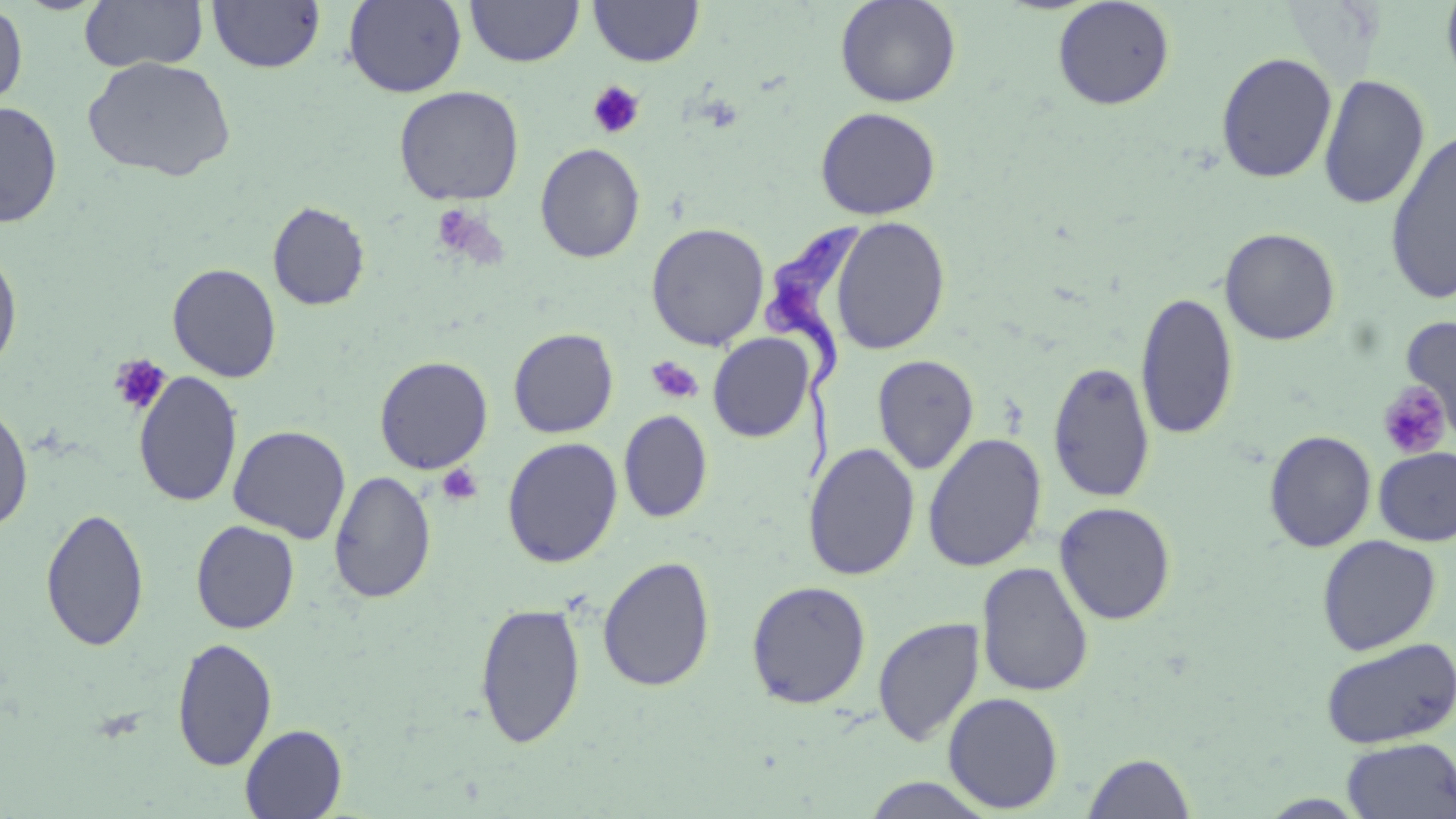
Approximate bounding boxes as named x1/y1/x2/y2 corners in pixels. Uninfected red blood cell locations: (x1=80, y1=0, x2=208, y2=72), (x1=207, y1=0, x2=326, y2=74), (x1=343, y1=0, x2=468, y2=98), (x1=465, y1=0, x2=583, y2=67), (x1=834, y1=0, x2=962, y2=107), (x1=1052, y1=0, x2=1175, y2=111), (x1=1441, y1=0, x2=1456, y2=93), (x1=589, y1=1, x2=704, y2=67), (x1=0, y1=3, x2=28, y2=109), (x1=1215, y1=51, x2=1337, y2=183), (x1=81, y1=56, x2=237, y2=182), (x1=1318, y1=73, x2=1431, y2=210), (x1=393, y1=85, x2=524, y2=206), (x1=0, y1=99, x2=63, y2=229), (x1=814, y1=106, x2=941, y2=220), (x1=1384, y1=127, x2=1456, y2=306), (x1=535, y1=142, x2=645, y2=263), (x1=267, y1=201, x2=370, y2=311), (x1=830, y1=216, x2=951, y2=356), (x1=646, y1=222, x2=770, y2=350), (x1=1219, y1=227, x2=1341, y2=346), (x1=0, y1=246, x2=23, y2=375), (x1=166, y1=263, x2=281, y2=383), (x1=1135, y1=291, x2=1238, y2=441), (x1=1398, y1=316, x2=1456, y2=442), (x1=508, y1=328, x2=618, y2=438), (x1=708, y1=333, x2=814, y2=442), (x1=872, y1=354, x2=979, y2=475), (x1=374, y1=355, x2=493, y2=474), (x1=1047, y1=361, x2=1155, y2=503), (x1=133, y1=372, x2=243, y2=508), (x1=0, y1=400, x2=34, y2=533), (x1=619, y1=409, x2=713, y2=523), (x1=228, y1=424, x2=351, y2=543), (x1=1263, y1=430, x2=1377, y2=553), (x1=922, y1=432, x2=1047, y2=573), (x1=501, y1=437, x2=623, y2=568), (x1=803, y1=443, x2=921, y2=581), (x1=1373, y1=447, x2=1456, y2=546), (x1=328, y1=470, x2=436, y2=604), (x1=1054, y1=501, x2=1177, y2=625), (x1=40, y1=507, x2=150, y2=652), (x1=190, y1=520, x2=299, y2=633), (x1=1316, y1=535, x2=1441, y2=655), (x1=597, y1=555, x2=716, y2=692), (x1=976, y1=561, x2=1094, y2=697), (x1=746, y1=580, x2=871, y2=709), (x1=475, y1=601, x2=586, y2=749), (x1=873, y1=617, x2=984, y2=746), (x1=172, y1=637, x2=278, y2=771), (x1=1320, y1=637, x2=1455, y2=749), (x1=943, y1=692, x2=1064, y2=813), (x1=240, y1=723, x2=347, y2=818), (x1=1342, y1=737, x2=1456, y2=818), (x1=1082, y1=751, x2=1197, y2=819), (x1=859, y1=776, x2=1001, y2=818). Trypanosoma brucei locations: (x1=759, y1=216, x2=866, y2=488). Platelet locations: (x1=588, y1=81, x2=645, y2=139), (x1=430, y1=204, x2=494, y2=262), (x1=107, y1=354, x2=171, y2=416), (x1=645, y1=356, x2=704, y2=405), (x1=1376, y1=381, x2=1452, y2=460), (x1=436, y1=463, x2=484, y2=506). Slide-level diagnosis: Trypanosoma brucei. Image is 1456×819 pixels. May-Grünwald-Giemsa-stained preparation. Single field of view. Captured at 1000x magnification. Thin blood smear. Light microscopy.